Report the malaria status of this cell.
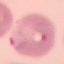

Parasitized.

Thin smear of blood. Giemsa stain. Cell patch, automatically extracted from a larger field of view and resized to 64 × 64 pixels. Photographed with a smartphone camera at the microscope eyepiece.